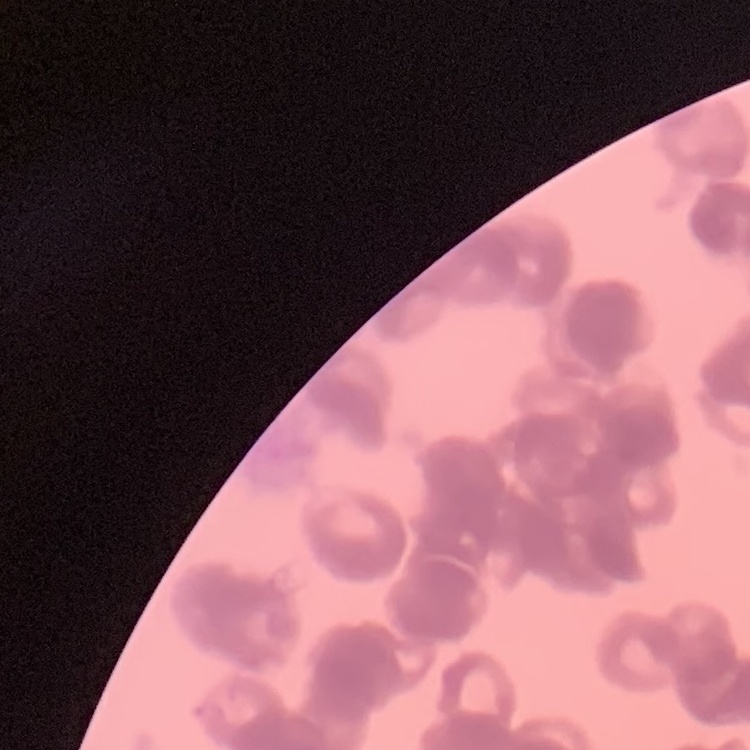
red blood cell morphology = rouleaux formation
stain = Field's or Giemsa
image type = one tile cut from a larger photomicrograph
preparation = thin blood film